Classify this cell by malaria status.
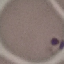
It is parasitized.

capture: smartphone through the microscope eyepiece
preparation: thin blood film
stain: Giemsa
image_type: cell patch, automatically extracted from a larger field of view and resized to 64 × 64 pixels